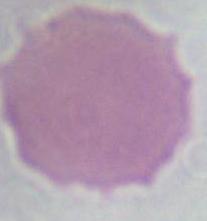
An erythrocyte is shown. Micrograph. Captured at 1000x magnification.